Point out each Plasmodium parasite.
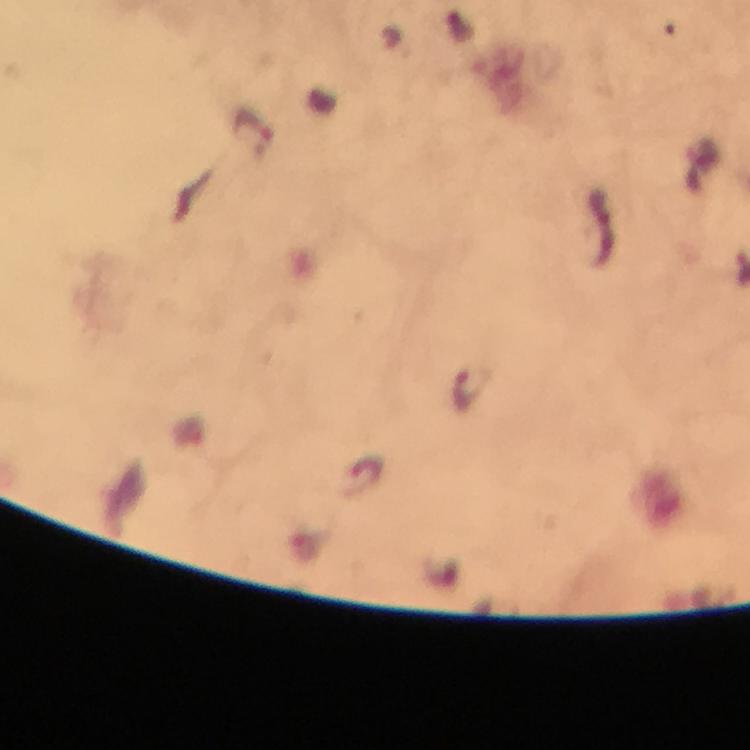
Approximate centers as (x, y) in pixels.
Plasmodium parasites: (254, 135), (471, 388).

Cropped region of a single field of view. Photographed through the microscope with a smartphone camera. From a diagnostic examination for malaria. Image is 750×750 pixels. 100x magnification. Immersion oil was used. Giemsa stain. Thick smear.